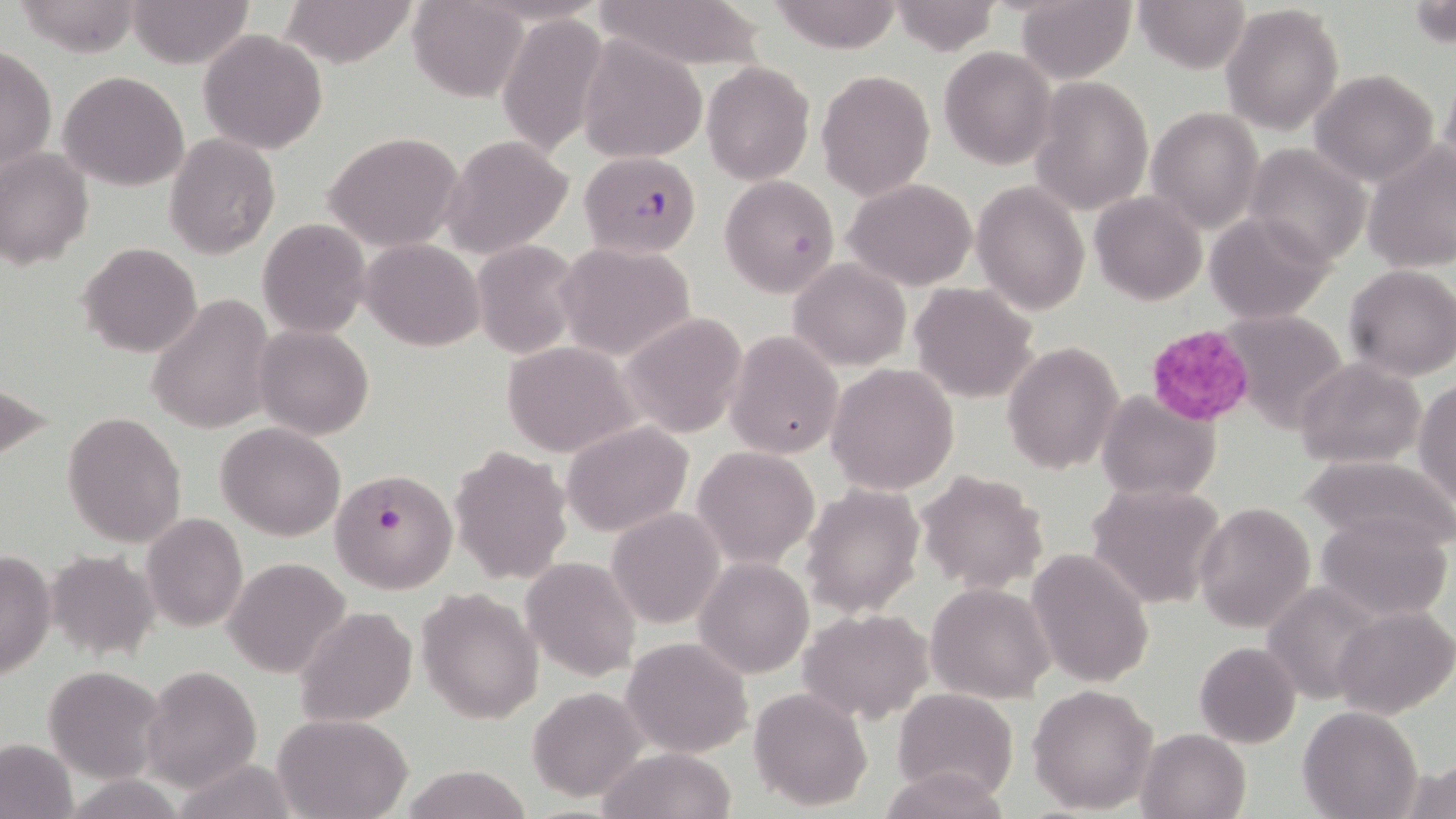
Approximate bounding boxes as (x1,y1)-(x2,y2) corner pairs in pixels. Plasmodium falciparum-infected red blood cell locations: (579,150)-(702,257), (327,467)-(458,592). Platelet locations: (1144,325)-(1253,426). Uninfected red blood cell locations: (13,0)-(146,56), (127,0)-(255,69), (279,0)-(419,67), (591,0)-(766,68), (891,0)-(998,54), (1016,0)-(1136,83), (1132,0)-(1251,74), (409,1)-(527,102), (769,1)-(903,52), (1408,1)-(1453,50), (1221,5)-(1344,134), (497,16)-(608,155), (198,30)-(328,154), (576,37)-(706,162), (1,46)-(55,176), (938,46)-(1055,170), (701,61)-(815,185), (1308,68)-(1441,187), (816,69)-(936,200), (58,70)-(189,191), (1029,75)-(1154,216), (1146,105)-(1264,235), (323,132)-(465,252), (165,133)-(279,259), (441,134)-(575,260), (1362,142)-(1456,274), (1243,144)-(1372,266), (0,148)-(94,269), (720,174)-(839,299), (843,179)-(979,291), (971,181)-(1089,317), (1090,192)-(1208,305), (1204,211)-(1337,324), (258,219)-(370,337), (362,239)-(484,351), (472,239)-(585,360), (556,242)-(697,362), (78,243)-(202,357), (787,258)-(910,370), (1342,265)-(1456,381), (750,267)-(877,409), (909,283)-(1039,402), (145,294)-(275,435), (1223,309)-(1348,434), (619,312)-(750,440), (254,324)-(374,440), (726,331)-(843,460), (503,342)-(638,456), (1003,342)-(1125,474), (1295,358)-(1425,470), (826,363)-(960,495), (0,378)-(54,469), (1414,379)-(1456,508), (1096,391)-(1221,501), (62,411)-(186,547), (562,421)-(694,536), (217,422)-(346,541), (449,444)-(574,585), (692,447)-(819,567), (1301,453)-(1455,552), (915,470)-(1049,593), (1086,482)-(1225,610), (801,483)-(924,616), (1193,501)-(1315,633), (606,509)-(725,629), (1316,512)-(1453,621), (141,513)-(248,631), (1026,548)-(1156,689), (0,550)-(55,681), (45,551)-(159,659), (520,555)-(641,681), (222,557)-(350,677), (694,558)-(814,677), (1261,581)-(1388,704), (925,582)-(1054,701), (417,587)-(544,724), (1333,605)-(1456,717), (296,607)-(417,728), (797,608)-(936,723), (622,637)-(752,757), (1195,641)-(1301,748), (43,665)-(166,784), (142,665)-(262,791), (1029,683)-(1158,813), (528,686)-(647,801), (749,688)-(873,812), (893,689)-(1018,801), (1298,706)-(1422,819), (274,714)-(413,819), (1137,727)-(1252,819), (0,736)-(79,819), (599,747)-(739,819), (1401,759)-(1456,818), (884,765)-(1008,819), (397,766)-(532,819). Slide-level diagnosis: Plasmodium falciparum. Optical microscopy. May-Grünwald-Giemsa stain. Thin blood film. 1000x magnification. Image is 1456×819 pixels. One field of a larger specimen.